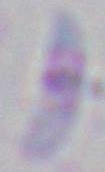

Captured at 1000x magnification. Photomicrograph. Toxoplasma gondii is seen.